Assess this cell for malaria.
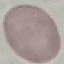
Uninfected.

stain = Giemsa
preparation = thin blood film
capture = smartphone camera at the microscope eyepiece
image type = cell patch, automatically extracted from a larger field of view and resized to 64 × 64 pixels